Point out each Plasmodium parasite.
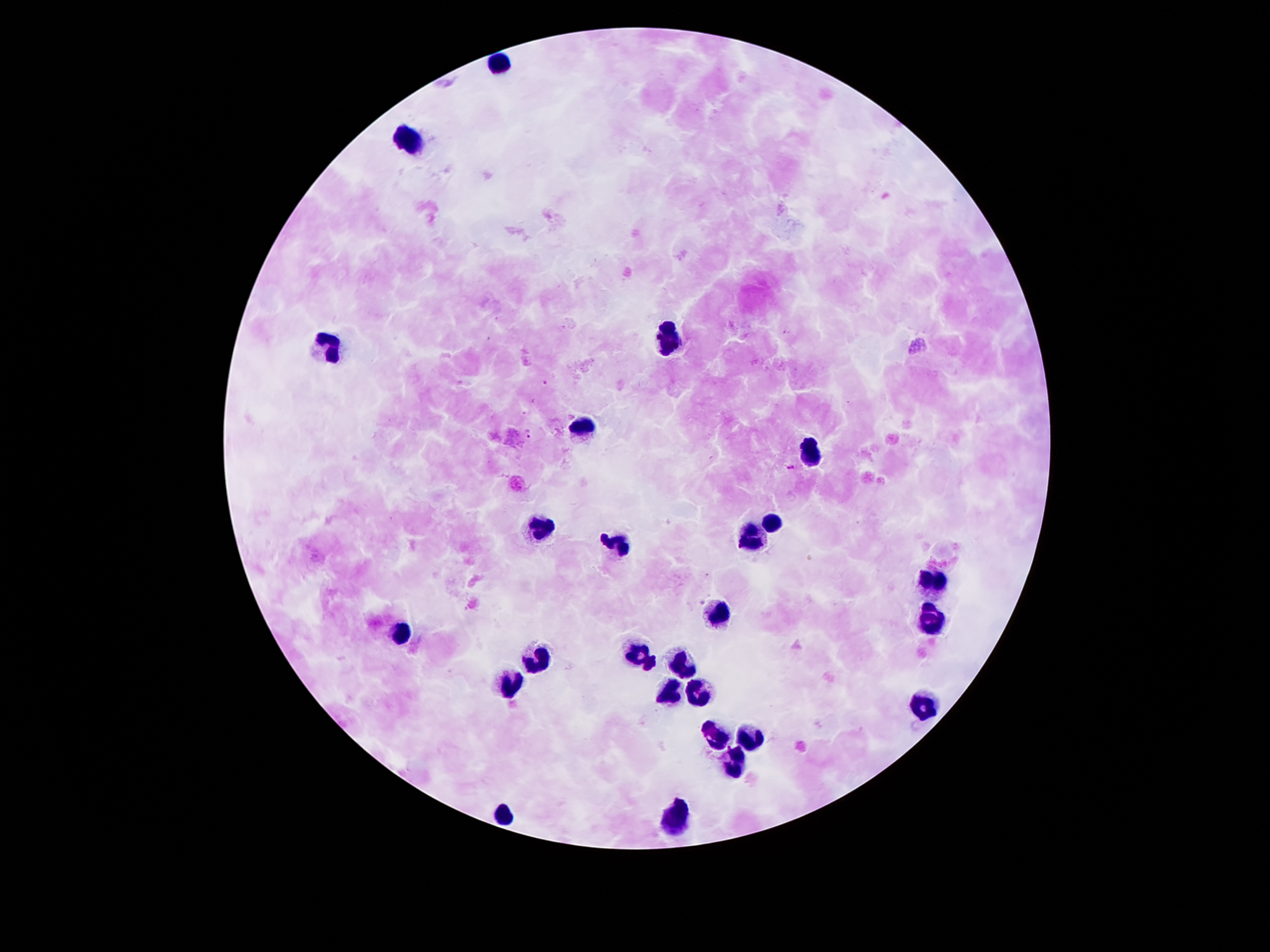

Approximate object centers, in pixels from the top-left corner.
Plasmodium parasites: (x=546, y=384), (x=529, y=433), (x=791, y=467).

Summary:
  - Leukocyte locations: (x=500, y=64), (x=410, y=141), (x=668, y=340), (x=325, y=347), (x=584, y=426), (x=809, y=449), (x=771, y=524), (x=537, y=528), (x=750, y=540), (x=618, y=542), (x=930, y=579), (x=718, y=613), (x=932, y=620), (x=403, y=633), (x=634, y=654), (x=537, y=660), (x=650, y=665), (x=680, y=667), (x=512, y=685), (x=702, y=692), (x=671, y=695), (x=927, y=706), (x=714, y=737), (x=752, y=738), (x=730, y=762), (x=505, y=814), (x=675, y=819)
  - Preparation: thick blood smear
  - Image size: 1270×952 pixels
  - Field of view: single
  - Patient malaria status: positive for Plasmodium falciparum
  - Capture: smartphone through the microscope eyepiece
  - Stain: Giemsa
  - Magnification: 100x